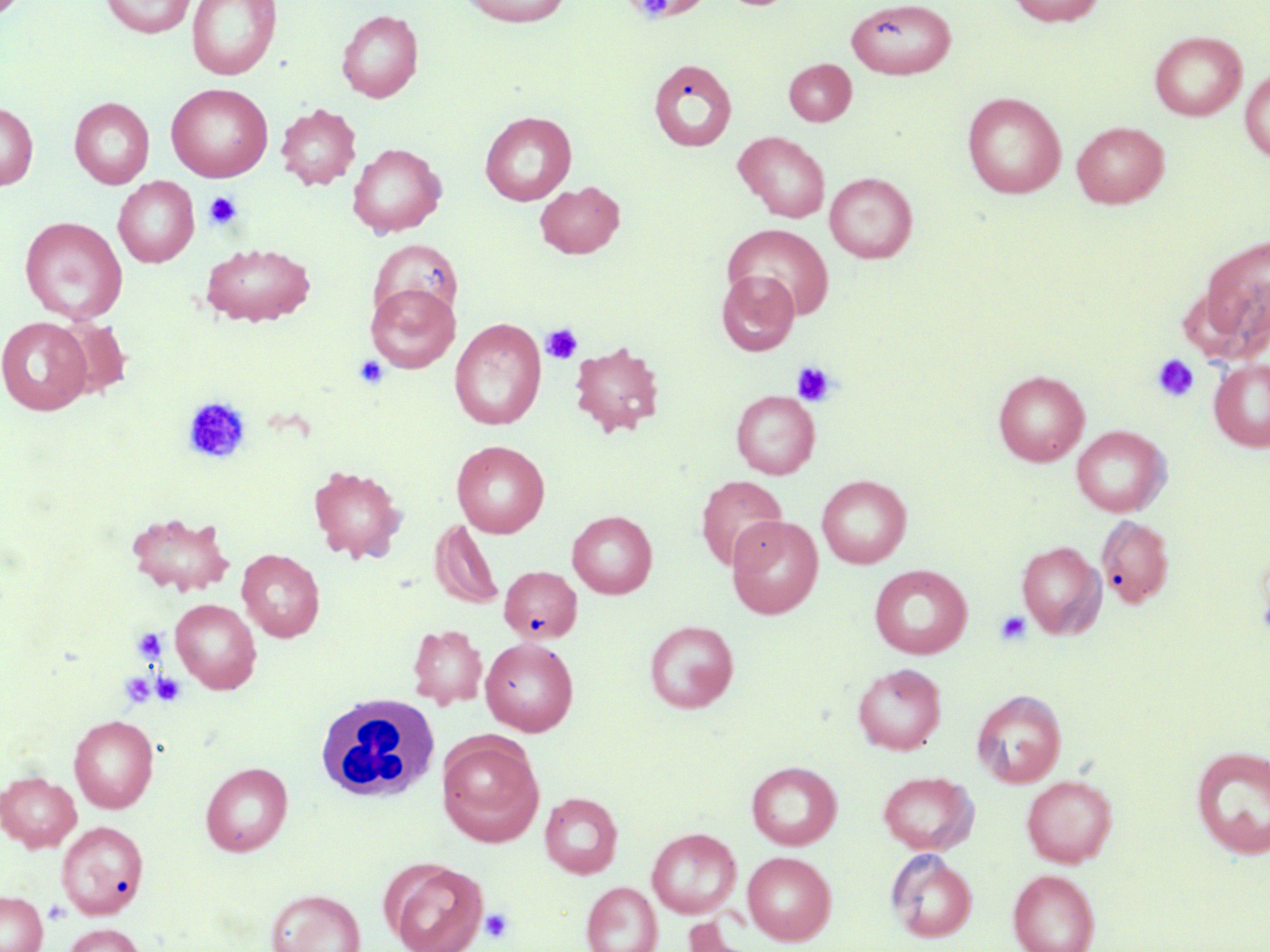

Summary:
  - Coordinate format: approximate bounding boxes as named x1/y1/x2/y2 corners in pixels
  - Uninfected red blood cell locations: (x1=101, y1=0, x2=195, y2=38), (x1=187, y1=0, x2=281, y2=80), (x1=458, y1=0, x2=572, y2=26), (x1=1007, y1=0, x2=1106, y2=27), (x1=846, y1=1, x2=956, y2=79), (x1=337, y1=9, x2=423, y2=102), (x1=1149, y1=31, x2=1246, y2=121), (x1=649, y1=58, x2=737, y2=153), (x1=784, y1=59, x2=856, y2=126), (x1=1240, y1=67, x2=1270, y2=162), (x1=166, y1=83, x2=273, y2=182), (x1=962, y1=92, x2=1066, y2=198), (x1=69, y1=97, x2=155, y2=189), (x1=0, y1=101, x2=37, y2=191), (x1=276, y1=104, x2=361, y2=190), (x1=480, y1=111, x2=577, y2=205), (x1=1071, y1=121, x2=1169, y2=208), (x1=734, y1=131, x2=830, y2=222), (x1=347, y1=143, x2=446, y2=237), (x1=825, y1=172, x2=917, y2=263), (x1=113, y1=177, x2=199, y2=267), (x1=535, y1=181, x2=625, y2=258), (x1=20, y1=216, x2=127, y2=323), (x1=723, y1=223, x2=834, y2=319), (x1=1192, y1=234, x2=1269, y2=359), (x1=369, y1=238, x2=462, y2=326), (x1=201, y1=243, x2=314, y2=326), (x1=716, y1=269, x2=800, y2=356), (x1=366, y1=283, x2=460, y2=373), (x1=0, y1=316, x2=92, y2=415), (x1=54, y1=318, x2=132, y2=399), (x1=450, y1=318, x2=547, y2=431), (x1=569, y1=341, x2=665, y2=437), (x1=1209, y1=359, x2=1270, y2=451), (x1=993, y1=370, x2=1089, y2=466), (x1=731, y1=390, x2=820, y2=479), (x1=1072, y1=425, x2=1170, y2=516), (x1=452, y1=440, x2=550, y2=538), (x1=307, y1=465, x2=407, y2=563), (x1=696, y1=475, x2=787, y2=572), (x1=817, y1=475, x2=911, y2=568), (x1=126, y1=511, x2=235, y2=597), (x1=567, y1=511, x2=657, y2=598), (x1=1096, y1=514, x2=1175, y2=609), (x1=727, y1=515, x2=823, y2=618), (x1=429, y1=519, x2=503, y2=610), (x1=1017, y1=541, x2=1105, y2=638), (x1=1255, y1=546, x2=1270, y2=649), (x1=237, y1=549, x2=325, y2=641), (x1=869, y1=564, x2=972, y2=658), (x1=499, y1=566, x2=582, y2=644), (x1=170, y1=599, x2=262, y2=694), (x1=644, y1=620, x2=739, y2=712), (x1=408, y1=624, x2=488, y2=709), (x1=480, y1=637, x2=578, y2=736), (x1=853, y1=663, x2=946, y2=754), (x1=972, y1=689, x2=1066, y2=787), (x1=68, y1=715, x2=159, y2=813), (x1=437, y1=734, x2=544, y2=846), (x1=1190, y1=745, x2=1270, y2=860), (x1=747, y1=761, x2=842, y2=849), (x1=200, y1=762, x2=293, y2=856), (x1=0, y1=771, x2=81, y2=851), (x1=878, y1=771, x2=978, y2=854), (x1=1021, y1=775, x2=1117, y2=867), (x1=540, y1=792, x2=623, y2=878), (x1=56, y1=820, x2=149, y2=919), (x1=647, y1=828, x2=741, y2=918), (x1=886, y1=849, x2=977, y2=943), (x1=743, y1=851, x2=836, y2=945), (x1=385, y1=859, x2=487, y2=952), (x1=1008, y1=869, x2=1100, y2=952), (x1=581, y1=882, x2=662, y2=952), (x1=265, y1=888, x2=366, y2=952), (x1=0, y1=891, x2=47, y2=952), (x1=63, y1=923, x2=146, y2=952)
  - Platelet locations: (x1=203, y1=191, x2=242, y2=230), (x1=541, y1=324, x2=582, y2=364), (x1=353, y1=354, x2=389, y2=389), (x1=1151, y1=354, x2=1200, y2=403), (x1=790, y1=361, x2=837, y2=407), (x1=183, y1=397, x2=252, y2=464), (x1=994, y1=610, x2=1032, y2=646), (x1=132, y1=628, x2=168, y2=664), (x1=118, y1=672, x2=156, y2=708), (x1=151, y1=672, x2=186, y2=707), (x1=43, y1=898, x2=72, y2=924), (x1=479, y1=907, x2=514, y2=945)
  - White blood cell locations: (x1=316, y1=692, x2=440, y2=802)
  - Slide-level diagnosis: negative for blood parasites
  - Magnification: 1000x
  - Stain: May-Grünwald-Giemsa
  - Preparation: thin blood smear
  - Image size: 1270×952 pixels
  - Modality: light microscopy
  - Field of view: single